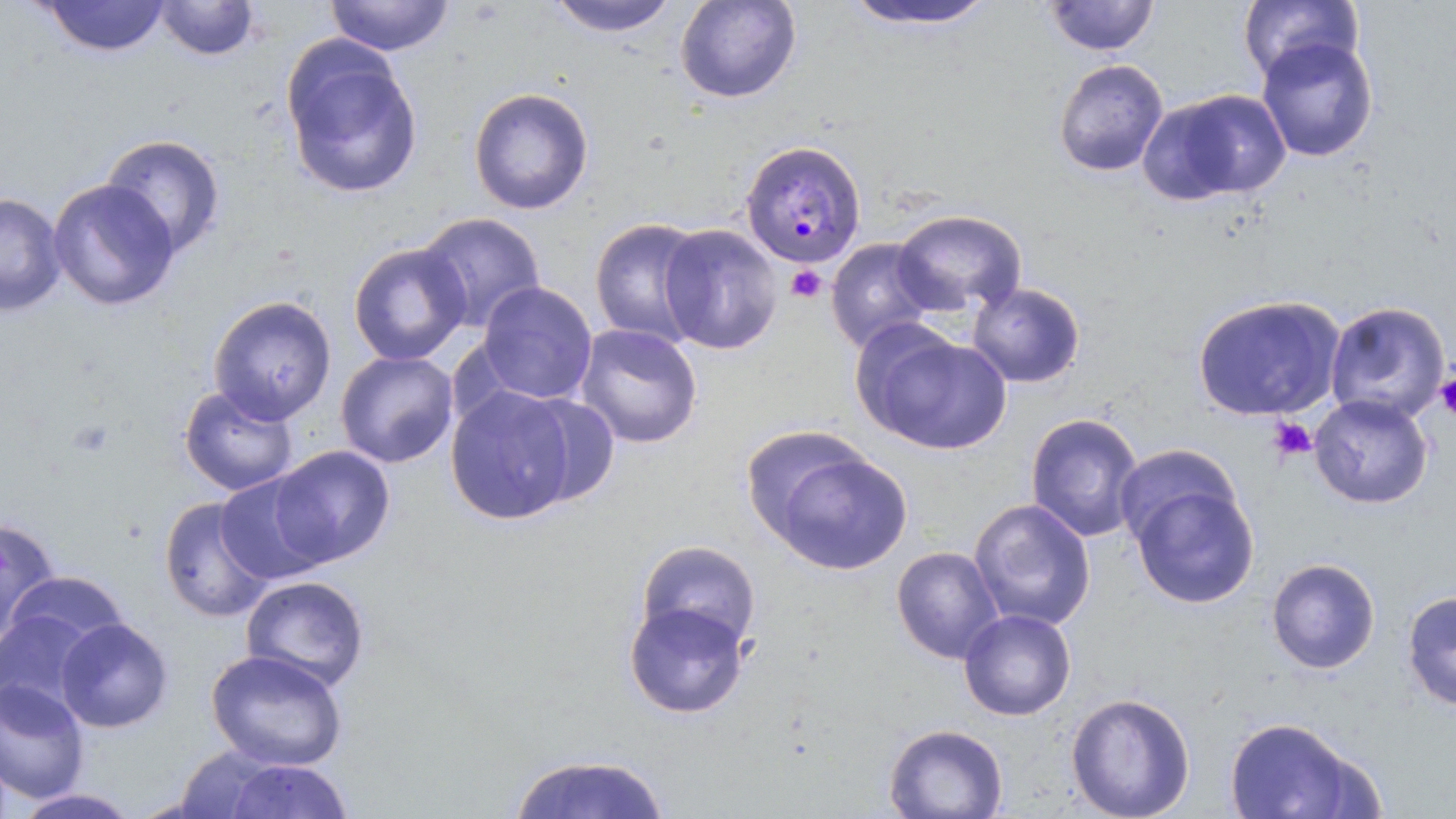
Approximate bounding boxes as (x1,y1)-(x2,y2) corner pairs in pixels. Uninfected red blood cell locations: (38,0)-(171,58), (155,0)-(262,61), (324,0)-(455,56), (674,0)-(802,104), (1041,0)-(1161,56), (1236,0)-(1364,86), (543,1)-(684,37), (840,1)-(1000,33), (280,36)-(424,200), (1255,36)-(1379,162), (1052,59)-(1169,178), (468,87)-(594,215), (1141,88)-(1291,205), (99,133)-(226,259), (47,179)-(180,311), (0,191)-(67,317), (890,209)-(1028,316), (415,211)-(547,333), (589,216)-(710,348), (659,222)-(783,355), (825,238)-(941,354), (348,241)-(471,366), (477,281)-(598,404), (967,282)-(1086,388), (1191,294)-(1347,423), (207,295)-(337,425), (1324,301)-(1451,424), (574,323)-(703,449), (856,324)-(1013,455), (335,350)-(459,468), (179,384)-(300,496), (444,384)-(580,526), (515,393)-(620,507), (1309,393)-(1433,509), (1025,412)-(1145,542), (738,424)-(874,543), (1112,443)-(1239,555), (268,444)-(396,568), (767,448)-(914,576), (214,473)-(332,586), (1129,481)-(1260,609), (158,495)-(276,622), (968,498)-(1096,631), (0,516)-(62,644), (636,540)-(762,652), (891,546)-(1004,664), (1265,557)-(1381,674), (5,570)-(128,658), (241,575)-(370,692), (1401,589)-(1456,711), (623,600)-(750,718), (0,607)-(106,722), (958,608)-(1077,720), (55,618)-(174,733), (206,649)-(348,771), (0,679)-(90,804), (1065,692)-(1195,819), (1222,716)-(1375,819), (883,724)-(1008,818), (172,745)-(281,818), (507,753)-(672,818), (222,758)-(353,818), (11,788)-(137,817). Plasmodium malariae-infected red blood cell locations: (740,138)-(867,269). Platelet locations: (785,264)-(827,304), (1436,372)-(1456,420), (68,418)-(115,458), (1268,418)-(1317,462). Slide-level diagnosis: Plasmodium malariae. Thin blood film. Image is 1456×819 pixels. Captured at 1000x magnification. Optical microscopy. May-Grünwald-Giemsa-stained preparation. Single field of view.